Identify the cell.
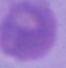
An erythrocyte.

Summary:
  - Modality: micrograph
  - Magnification: 1000x